Name the parasite shown.
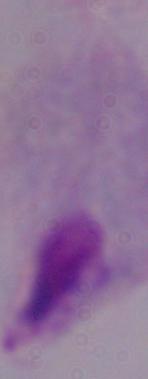

This is a trichomonad.

modality = micrograph
magnification = 1000x